Outline platelets.
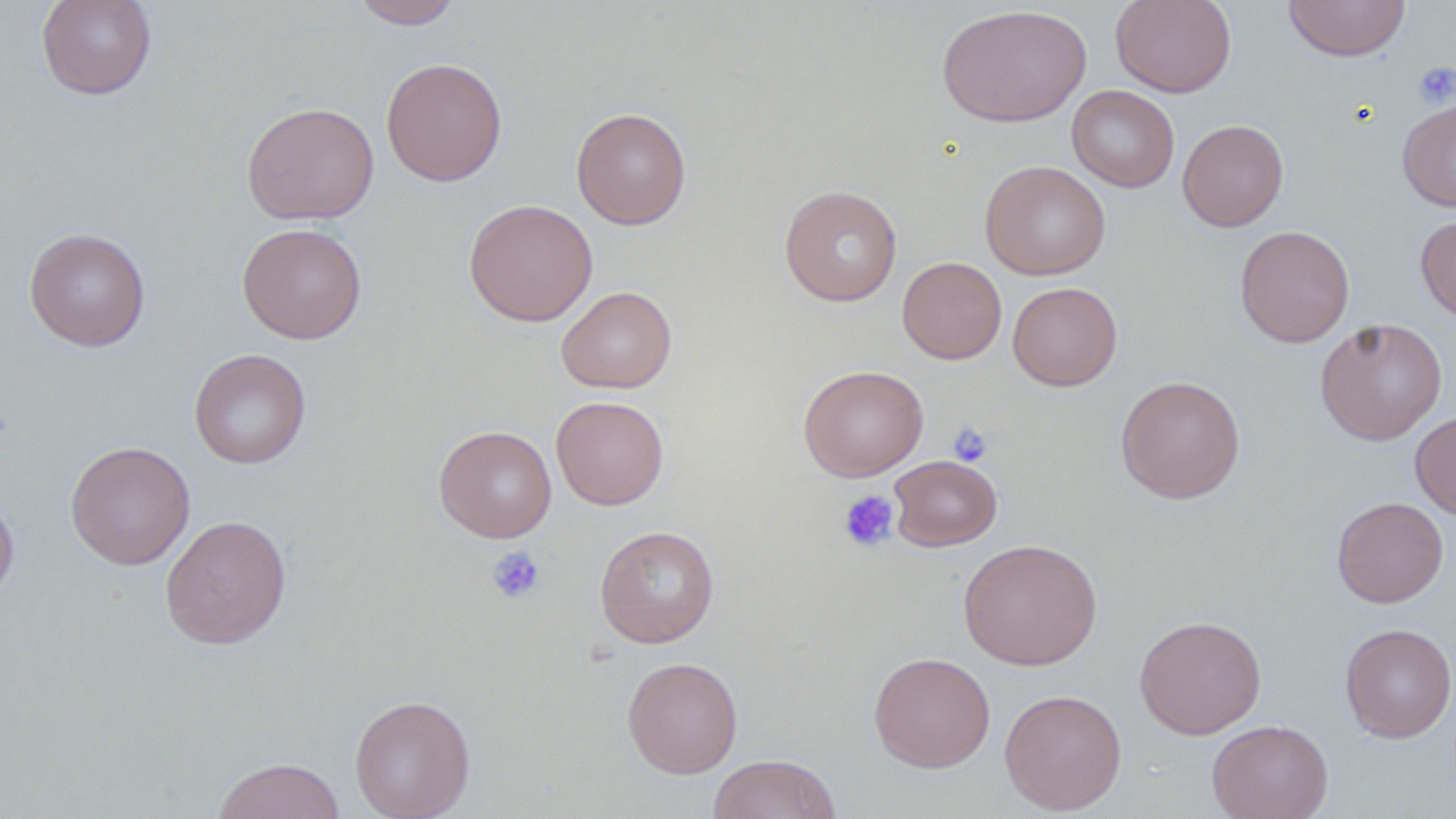
Approximate bounding boxes as (x1, y1, x2, y2) in pixels.
Platelets: (1413, 61, 1456, 108), (947, 422, 993, 467), (838, 489, 899, 552), (486, 545, 546, 604).

Uninfected red blood cell locations: (36, 0, 157, 100), (349, 0, 465, 29), (1110, 0, 1236, 97), (1283, 1, 1411, 62), (936, 4, 1091, 128), (381, 57, 508, 186), (1066, 85, 1180, 192), (1397, 97, 1456, 212), (241, 101, 379, 225), (571, 106, 692, 230), (1177, 119, 1289, 232), (979, 160, 1111, 280), (779, 185, 903, 306), (463, 198, 598, 327), (1415, 213, 1456, 323), (237, 223, 367, 344), (1234, 225, 1355, 348), (24, 227, 151, 352), (897, 256, 1007, 364), (1008, 281, 1122, 391), (556, 286, 677, 393), (1315, 317, 1448, 445), (189, 348, 312, 469), (798, 364, 928, 482), (1115, 375, 1246, 503), (551, 396, 668, 510), (1410, 410, 1456, 521), (433, 425, 557, 542), (65, 440, 195, 569), (888, 455, 1002, 551), (0, 491, 19, 603), (1332, 496, 1448, 607), (160, 514, 292, 649), (594, 524, 720, 648), (957, 538, 1104, 671), (1134, 614, 1267, 740), (1339, 623, 1456, 742), (868, 651, 996, 772), (622, 656, 743, 778), (999, 688, 1128, 815), (349, 694, 475, 819), (1207, 719, 1333, 819), (708, 753, 843, 818), (211, 757, 346, 819). Slide-level diagnosis: negative for blood parasites. 1000x magnification. Optical microscopy. Single field of view. Thin blood smear. Image is 1456×819 pixels. May-Grünwald-Giemsa stain.